Assess this cell for malaria.
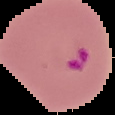

Parasitized.

image size = 115×115 pixels
preparation = thin blood film
image type = segmented cell region with the area outside set to black